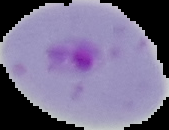

{
  "image_type": "cell region segmented out of the field of view; surrounding area masked to black",
  "image_size": "169×130 pixels",
  "preparation": "thin blood smear",
  "result": "malaria parasites identified"
}